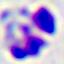

identification: leukocyte
modality: micrograph
magnification: 400x